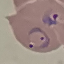
Summary:
  - Malaria status: parasitized
  - Stain: Giemsa
  - Preparation: thin smear
  - Image type: automatically extracted cell patch, resized to 64 × 64 pixels
  - Capture: smartphone camera at the microscope eyepiece